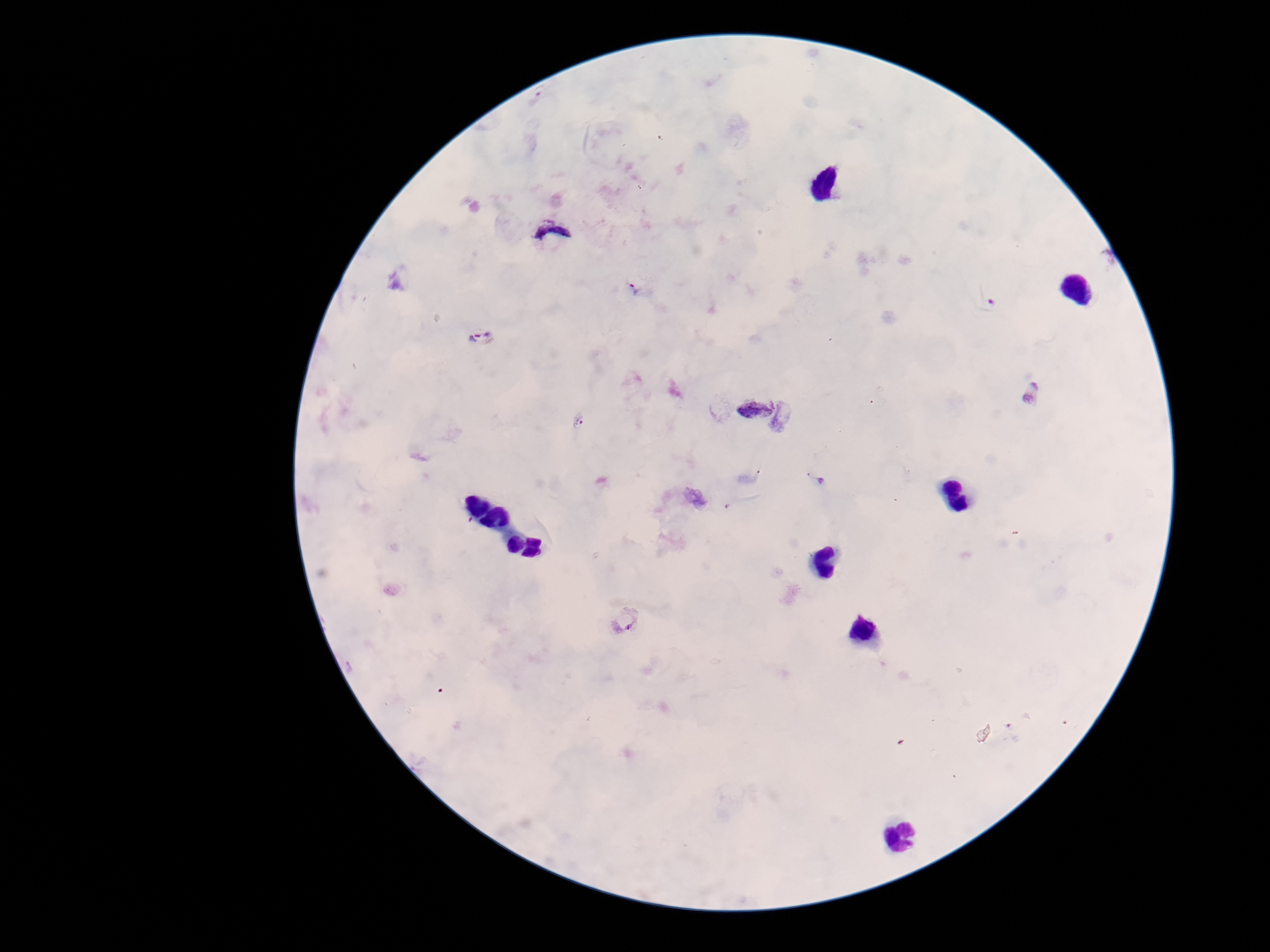 Approximate object centers, in pixels from the top-left corner. Plasmodium parasite locations: (x=549, y=232), (x=634, y=290), (x=988, y=305), (x=479, y=337), (x=1032, y=393), (x=754, y=406), (x=579, y=421), (x=814, y=479), (x=627, y=619). Thick peripheral-blood smear. 100x magnification. Giemsa stain. Image is 1270×952 pixels. One field from this slide. Patient malaria status: positive. Smartphone photograph taken through the microscope eyepiece.